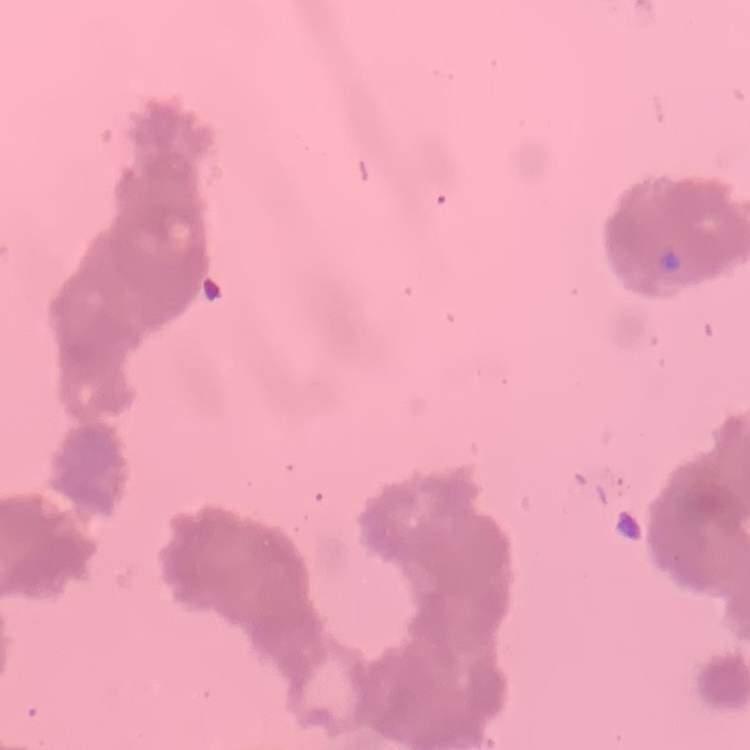

{
  "erythrocyte_morphology": "rouleaux formation",
  "image_type": "one tile cut from a larger photomicrograph",
  "stain": "Field's or Giemsa",
  "preparation": "thin blood smear"
}